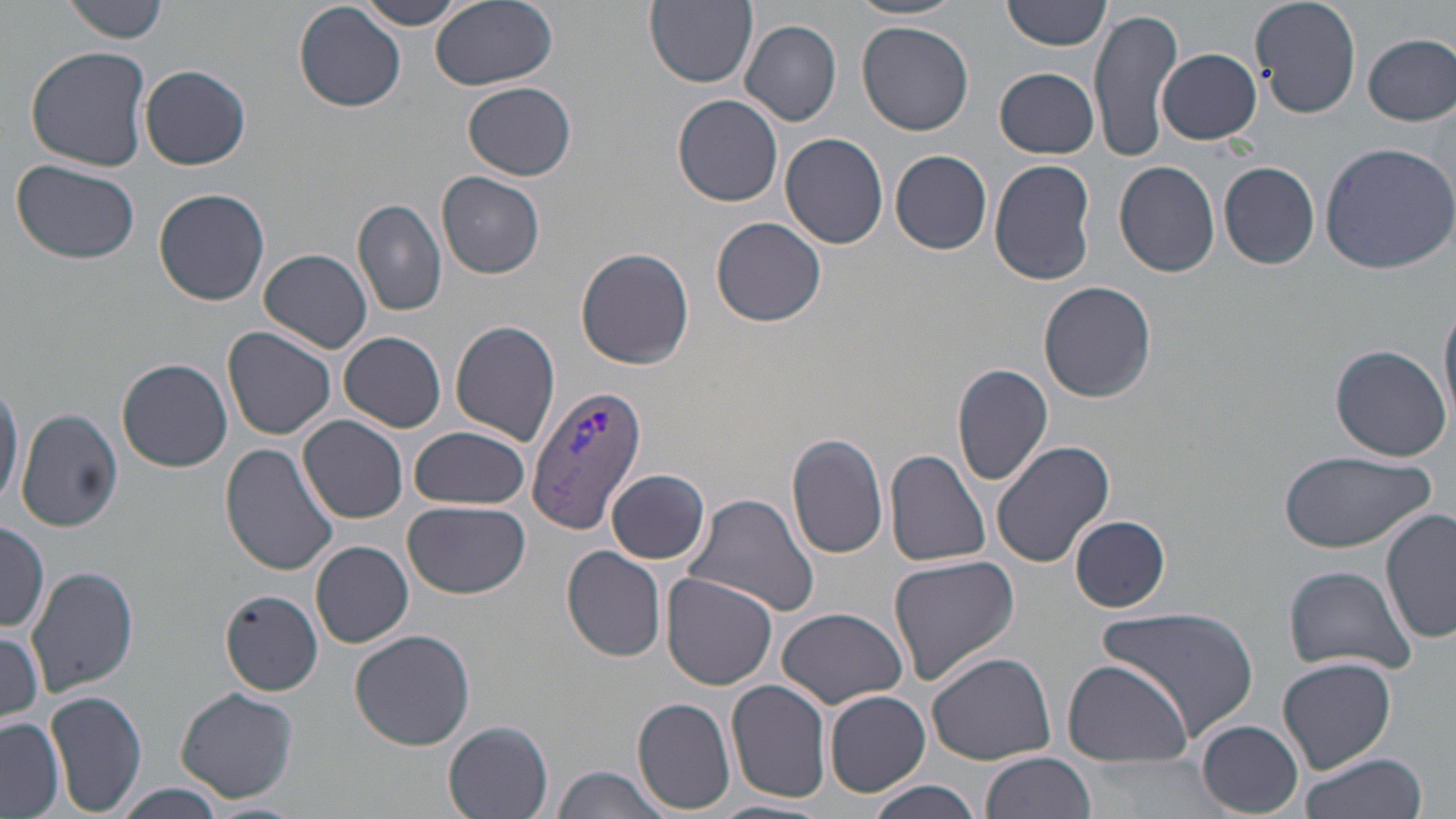
Summary:
  - Coordinate format: approximate bounding boxes as [x1, y1, x2, y2] in pixels
  - Uninfected red blood cell locations: [64, 0, 172, 43], [357, 0, 470, 30], [429, 0, 557, 91], [645, 0, 758, 89], [1004, 0, 1111, 52], [1251, 0, 1362, 118], [847, 1, 967, 22], [295, 3, 405, 113], [1091, 5, 1182, 164], [740, 20, 842, 126], [855, 22, 974, 135], [1363, 33, 1455, 125], [23, 45, 152, 173], [1156, 48, 1261, 145], [139, 66, 251, 169], [994, 67, 1099, 158], [464, 82, 578, 179], [672, 94, 783, 207], [779, 132, 889, 250], [1319, 140, 1456, 274], [891, 150, 993, 253], [988, 158, 1097, 285], [11, 160, 141, 266], [1115, 160, 1220, 277], [1218, 161, 1319, 269], [437, 173, 546, 279], [154, 188, 270, 305], [351, 199, 447, 317], [711, 216, 827, 328], [575, 247, 695, 370], [260, 249, 372, 353], [1037, 281, 1157, 403], [1439, 294, 1456, 433], [450, 320, 561, 446], [223, 326, 337, 439], [340, 332, 447, 431], [1330, 345, 1451, 460], [118, 358, 233, 472], [953, 363, 1053, 486], [0, 382, 23, 511], [16, 408, 123, 532], [300, 415, 409, 523], [410, 424, 531, 512], [787, 432, 890, 559], [990, 440, 1115, 568], [220, 443, 340, 577], [885, 448, 991, 568], [1279, 449, 1436, 555], [607, 468, 711, 565], [682, 493, 819, 618], [404, 499, 530, 598], [1382, 509, 1456, 646], [1070, 514, 1171, 613], [0, 520, 50, 633], [311, 541, 414, 649], [562, 545, 666, 662], [887, 555, 1020, 686], [1283, 563, 1416, 676], [28, 567, 139, 697], [662, 574, 778, 691], [217, 587, 325, 694], [777, 606, 909, 708], [1099, 607, 1260, 739], [0, 625, 44, 730], [349, 629, 477, 749], [927, 651, 1056, 765], [1278, 657, 1398, 772], [1060, 659, 1193, 769], [726, 681, 832, 804], [176, 686, 299, 803], [45, 690, 148, 816], [823, 690, 931, 798], [633, 696, 736, 813], [0, 717, 64, 818], [1197, 720, 1304, 815], [444, 722, 555, 818], [983, 751, 1097, 819], [1297, 753, 1426, 819], [549, 765, 669, 819], [865, 780, 984, 819], [107, 783, 231, 816], [707, 798, 833, 819]
  - Plasmodium vivax-infected red blood cell locations: [528, 384, 646, 535]
  - Slide-level diagnosis: Plasmodium vivax
  - Stain: May-Grünwald-Giemsa
  - Field of view: one of a larger specimen
  - Image size: 1456×819 pixels
  - Magnification: 1000x
  - Preparation: thin blood smear
  - Modality: light microscopy